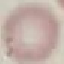

Result: no malaria parasites seen. Photographed with a smartphone camera at the microscope eyepiece. Cell patch, automatically extracted from a larger field of view and resized to 64 × 64 pixels. Giemsa stain. Thin blood film.